State which cell type is depicted.
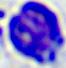

This is a leukocyte.

Summary:
  - Magnification: 400x
  - Modality: micrograph